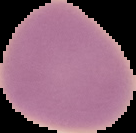
image type = segmented cell region on a black background
malaria status = uninfected
preparation = thin blood smear
image size = 136×133 pixels